Assess the morphology of the red blood cells.
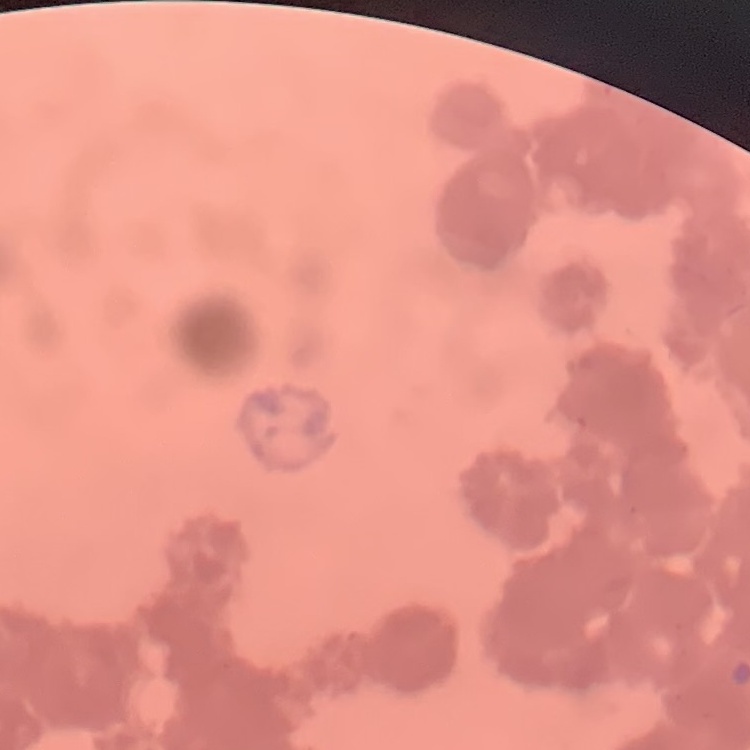
Rouleaux formation.

stain = Field's or Giemsa
image type = square crop of a larger photomicrograph
preparation = thin blood smear